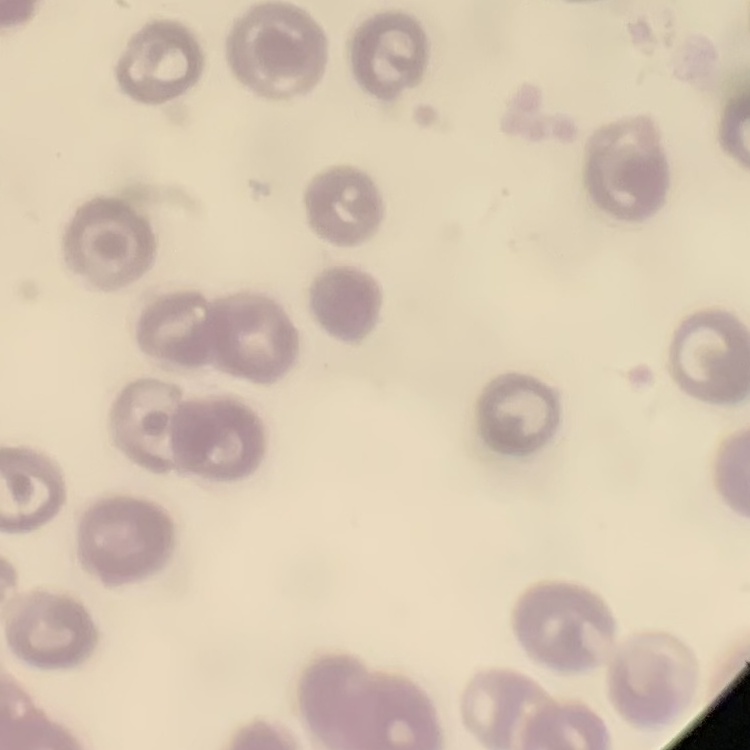 The red blood cells exhibit no rouleaux formation. One tile cut from a larger photomicrograph. Field's or Giemsa stain. Thin blood film.